Classify this cell by malaria status.
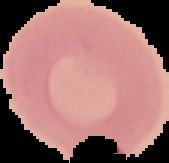
Uninfected.

preparation = thin blood film
image size = 169×163 pixels
image type = segmented cell region with the area outside set to black